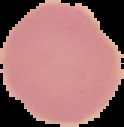

Malaria status: uninfected. Image is 124×127 pixels. From a thin blood smear. Segmented cell region on a black background.